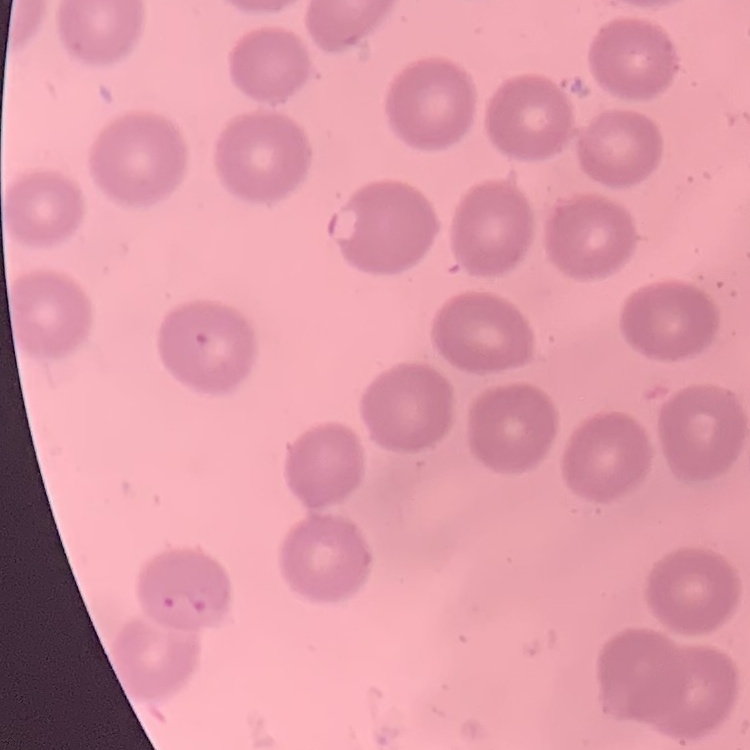
red blood cell morphology = no rouleaux formation
preparation = thin blood film
image type = square crop of a larger photomicrograph
stain = Field's or Giemsa